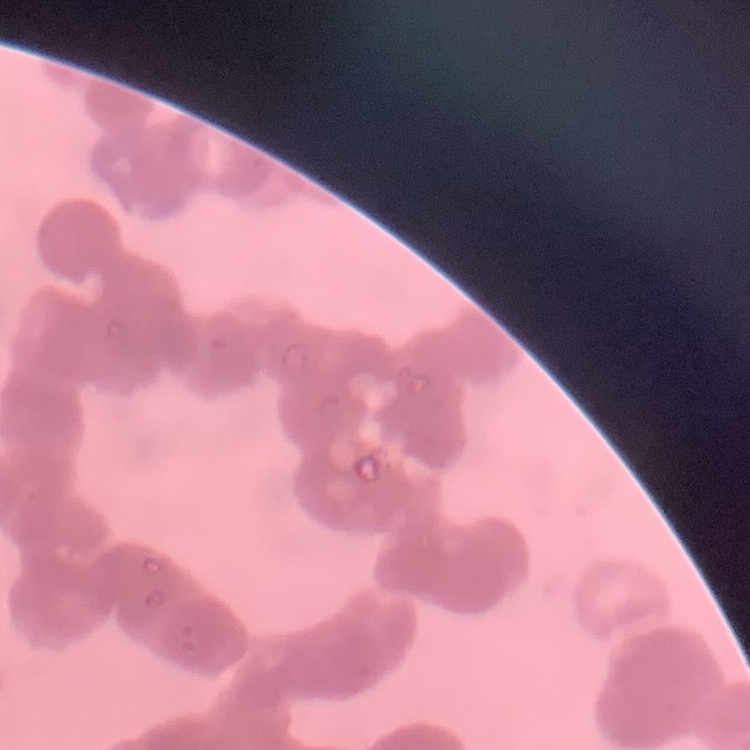 The red blood cells exhibit rouleaux formation. Thin peripheral smear. Square crop of a larger photomicrograph. Stained with either Field's or Giemsa.